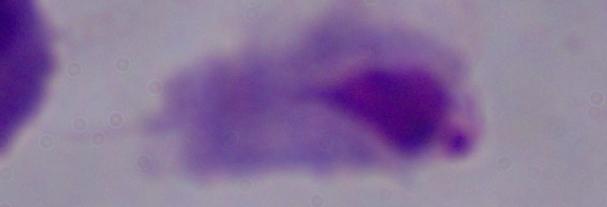 A trichomonad is seen. Photomicrograph. Captured at 1000x magnification.